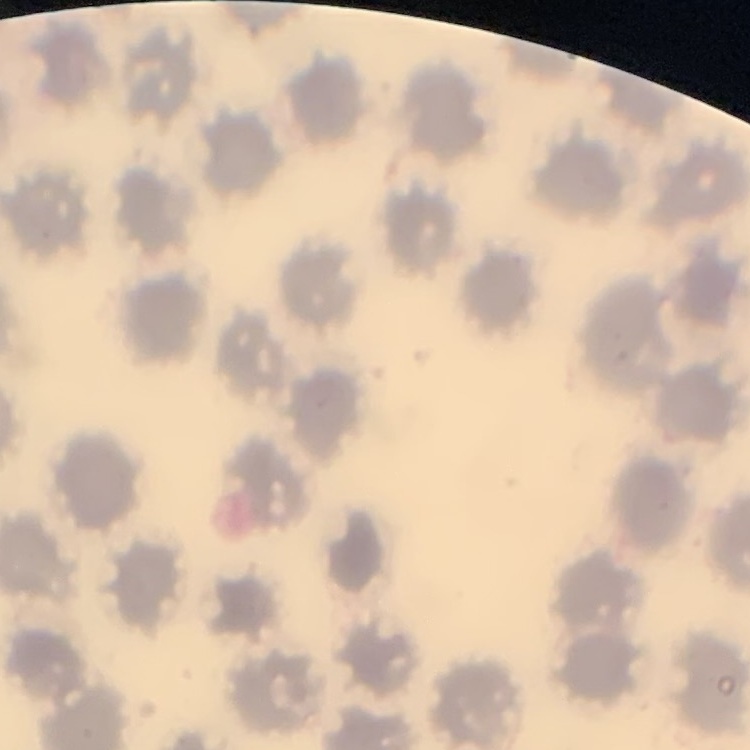
Summary:
  - Erythrocyte morphology: no rouleaux formation
  - Stain: Field's or Giemsa
  - Preparation: thin blood smear
  - Image type: square crop of a larger photomicrograph